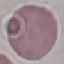

Summary:
  - Result: no malaria parasites seen
  - Capture: smartphone through the microscope eyepiece
  - Stain: Giemsa
  - Image type: cell patch, automatically extracted from a larger field of view and resized to 64 × 64 pixels
  - Preparation: thin blood smear